Locate and identify every blood parasite.
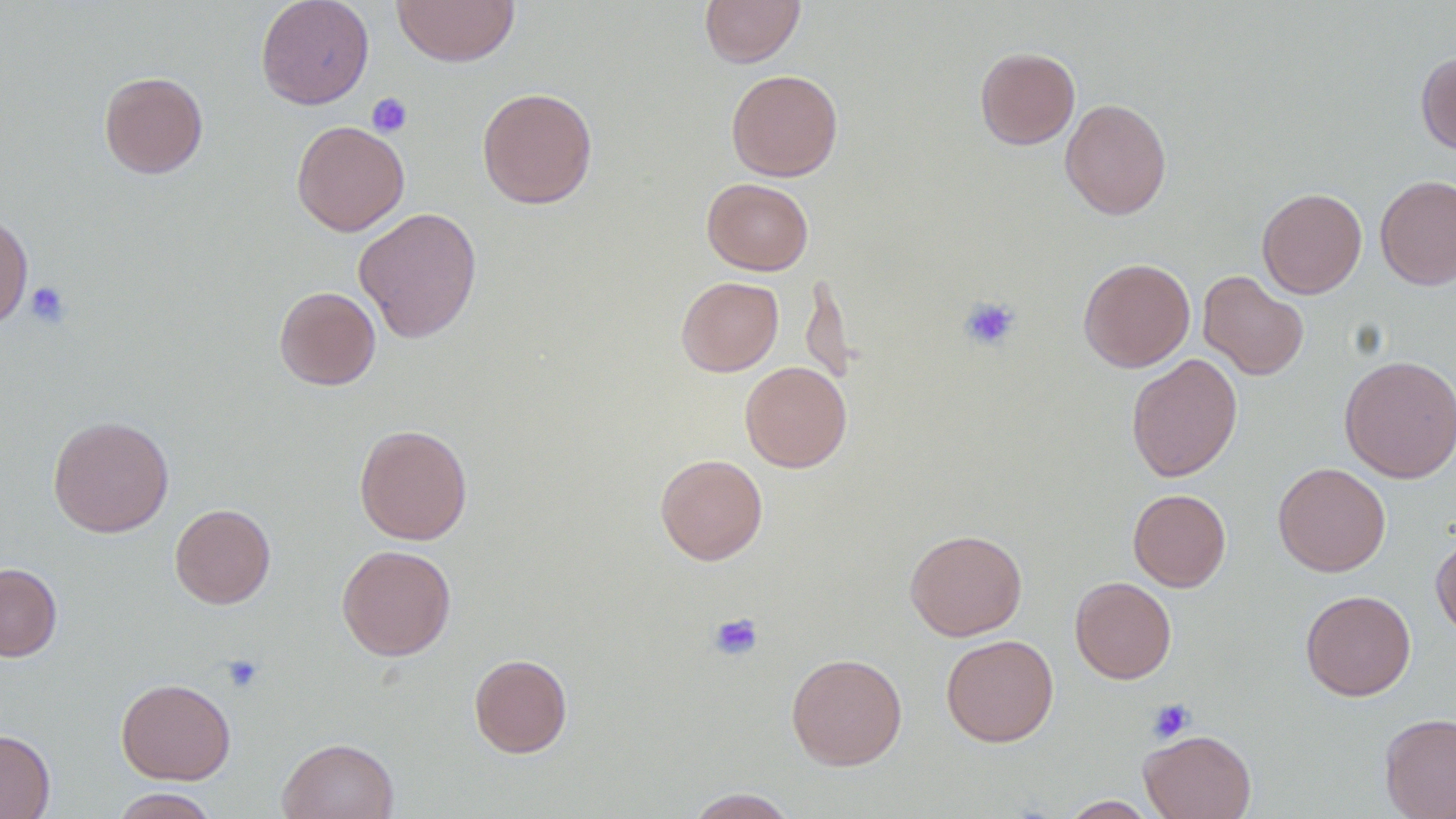
No blood parasites observed.

Summary:
  - Coordinate format: approximate bounding boxes as [x1, y1, x2, y2] in pixels
  - Platelet locations: [367, 92, 412, 137], [26, 281, 71, 329], [959, 296, 1021, 352], [708, 612, 764, 661], [221, 653, 264, 693], [1147, 698, 1195, 744]
  - Uninfected red blood cell locations: [255, 0, 374, 109], [392, 0, 520, 67], [699, 0, 804, 67], [975, 46, 1080, 149], [1416, 52, 1456, 155], [726, 69, 843, 181], [98, 71, 208, 178], [477, 86, 598, 209], [1060, 98, 1172, 220], [291, 120, 410, 236], [1375, 174, 1456, 291], [702, 178, 813, 275], [1256, 188, 1367, 298], [353, 207, 482, 343], [0, 212, 33, 330], [1078, 258, 1195, 372], [1198, 270, 1309, 380], [800, 272, 854, 388], [675, 276, 783, 376], [273, 286, 381, 390], [1126, 353, 1243, 482], [1339, 354, 1456, 484], [740, 361, 852, 472], [48, 414, 174, 538], [355, 424, 473, 545], [654, 453, 768, 565], [1273, 462, 1391, 576], [1128, 488, 1231, 592], [170, 503, 276, 609], [904, 528, 1027, 641], [1431, 533, 1456, 639], [336, 544, 456, 661], [0, 562, 62, 661], [1070, 577, 1176, 684], [1300, 590, 1416, 700], [941, 634, 1059, 746], [786, 652, 907, 770], [468, 653, 573, 758], [116, 678, 236, 784], [1379, 712, 1456, 819], [0, 728, 55, 819], [1139, 729, 1256, 819], [277, 738, 399, 819], [109, 787, 220, 818], [683, 787, 799, 818], [1057, 796, 1162, 818]
  - Slide-level diagnosis: negative for blood parasites
  - Field of view: one of a larger specimen
  - Preparation: thin blood smear
  - Modality: light microscopy
  - Image size: 1456×819 pixels
  - Magnification: 1000x